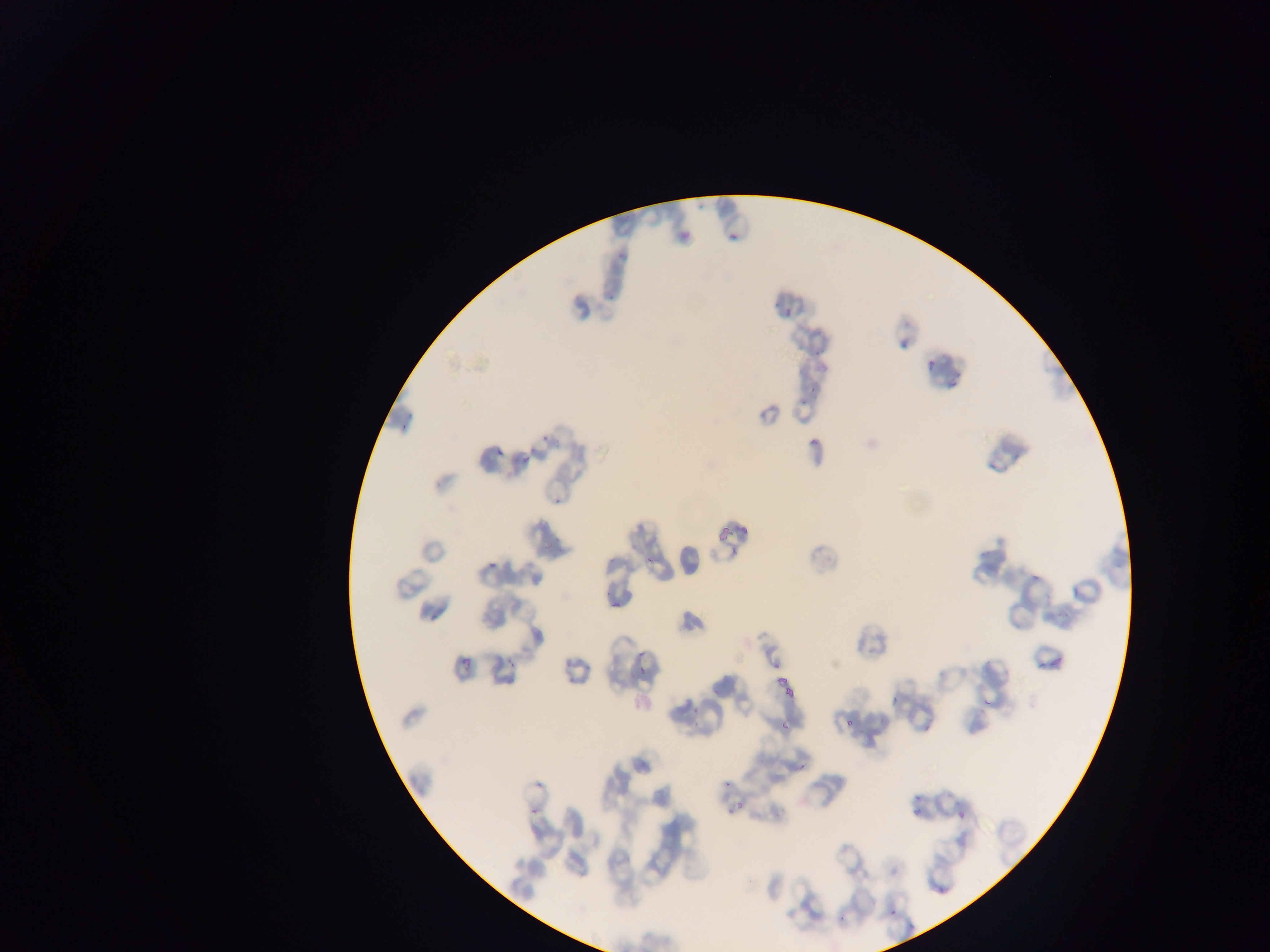

{
  "field_of_view": "single",
  "preparation": "thin blood film",
  "image_size": "1270×952 pixels",
  "plasmodium_parasite_locations": "approximate bounding boxes as {left, top, right, bottom} in pixels: {728, 231, 739, 242}, {771, 296, 781, 309}, {780, 305, 795, 316}, {895, 341, 908, 352}, {810, 347, 828, 357}, {924, 357, 939, 373}, {806, 381, 821, 393}, {798, 391, 808, 411}, {402, 410, 417, 417}, {394, 423, 404, 433}, {534, 423, 558, 447}, {805, 435, 820, 448}, {495, 445, 504, 459}, {520, 454, 530, 468}, {553, 493, 563, 506}, {715, 523, 735, 542}, {542, 540, 558, 551}, {727, 545, 739, 553}, {556, 546, 564, 560}, {642, 548, 663, 569}, {487, 561, 496, 569}, {1031, 571, 1041, 580}, {597, 586, 615, 597}, {605, 602, 623, 610}, {423, 612, 441, 622}, {459, 647, 474, 670}, {633, 649, 647, 656}, {1050, 649, 1064, 671}, {502, 658, 526, 672}, {1032, 663, 1038, 671}, {636, 668, 650, 677}, {776, 676, 799, 702}, {889, 689, 899, 707}, {983, 692, 994, 710}, {692, 704, 699, 719}, {844, 713, 859, 727}, {778, 719, 793, 734}, {795, 756, 811, 775}, {534, 779, 547, 794}, {909, 791, 923, 803}, {732, 798, 750, 812}, {727, 804, 741, 814}, {909, 804, 923, 820}, {952, 807, 969, 829}, {934, 887, 947, 899}, {838, 906, 850, 922}, {886, 907, 896, 918} | approximate {x, y} pixel centers of objects too small to bound: {727, 783}, {531, 813}",
  "country": "Ghana",
  "capture": "mobile-phone photograph through a microscope"
}